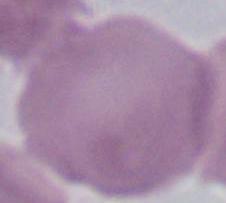
modality = micrograph
magnification = 1000x
identification = red blood cell